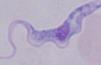

Photomicrograph. 1000x magnification. A trypanosome is shown.